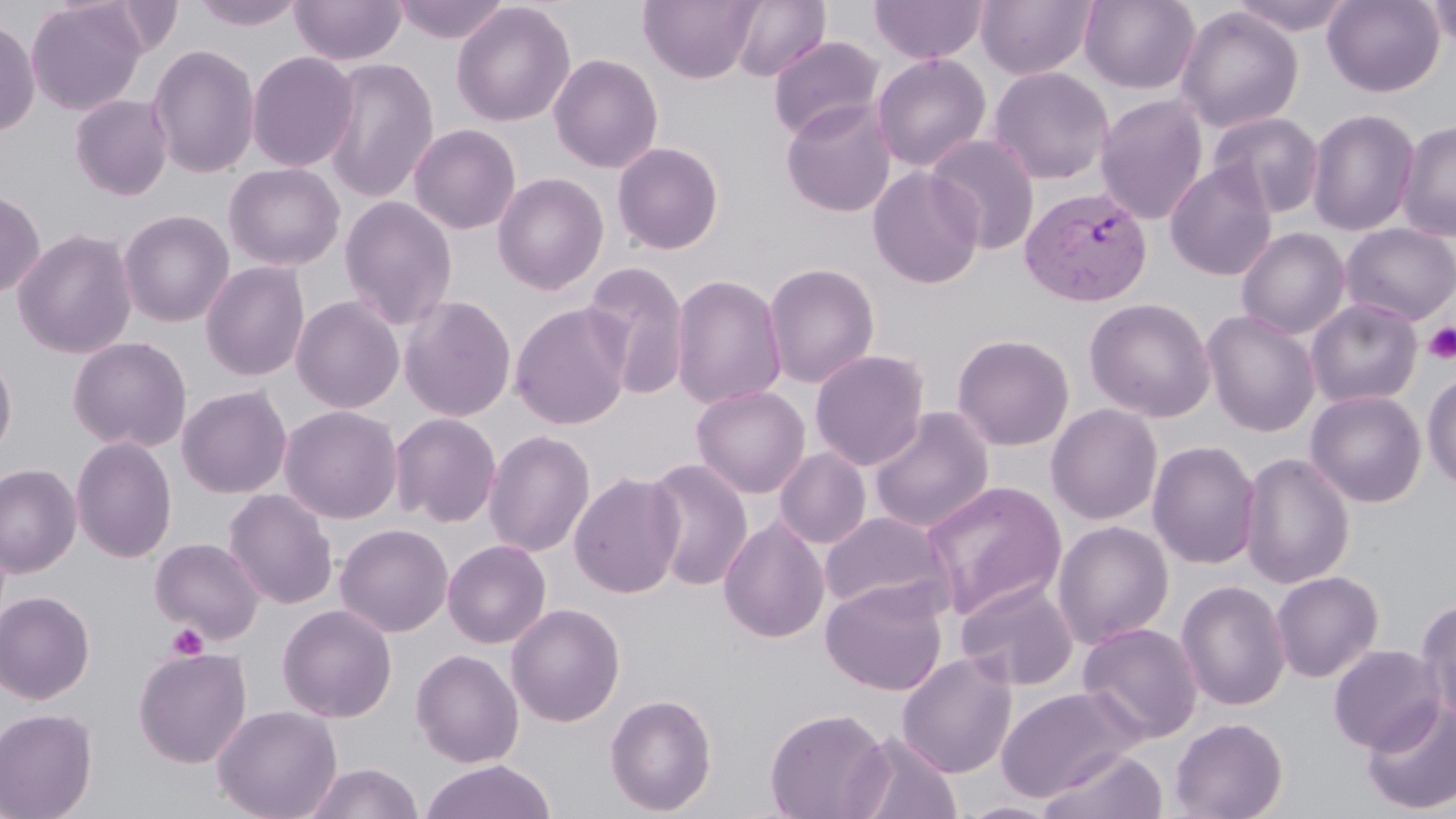
slide_level_diagnosis: Plasmodium vivax
platelet_locations: 'approximate bounding boxes as (x1,y1)-(x2,y2) corner pairs in pixels: (1423,322)-(1456,364), (167,622)-(209,659)'
preparation: thin blood smear
field_of_view: single
modality: light microscopy
image_size: 1456×819 pixels
uninfected_red_blood_cell_locations: 'approximate bounding boxes as (x1,y1)-(x2,y2) corner pairs in pixels: (25,0)-(147,115), (289,0)-(407,66), (392,0)-(509,44), (638,0)-(763,84), (868,0)-(988,64), (975,0)-(1096,81), (1079,0)-(1200,93), (1227,0)-(1358,35), (1322,0)-(1445,97), (1425,0)-(1456,51), (192,1)-(306,31), (729,1)-(830,82), (451,2)-(576,128), (1175,6)-(1303,133), (0,16)-(40,138), (768,36)-(885,143), (147,44)-(261,179), (246,50)-(360,172), (548,53)-(664,174), (871,53)-(992,172), (321,57)-(440,204), (987,66)-(1115,185), (69,94)-(173,201), (1095,94)-(1209,225), (780,100)-(898,218), (1306,108)-(1419,237), (1207,112)-(1325,219), (1396,119)-(1456,242), (409,124)-(521,234), (926,134)-(1041,254), (611,141)-(725,255), (223,162)-(346,271), (1165,162)-(1277,281), (866,166)-(985,290), (492,172)-(609,295), (500,172)-(615,429), (0,188)-(45,299), (339,195)-(457,329), (118,209)-(235,327), (1340,223)-(1456,326), (1236,227)-(1350,340), (12,228)-(137,359), (199,261)-(310,382), (582,261)-(690,400), (763,262)-(880,388), (670,273)-(787,411), (290,295)-(405,413), (398,295)-(517,422), (1083,297)-(1215,422), (1305,298)-(1423,408), (509,302)-(633,430), (1202,309)-(1320,436), (952,333)-(1075,451), (67,336)-(192,452), (0,348)-(18,462), (809,349)-(931,471), (1422,371)-(1456,489), (690,384)-(810,498), (176,385)-(293,498), (1305,389)-(1427,508), (1046,403)-(1162,525), (279,405)-(403,524), (868,407)-(994,534), (389,412)-(502,527), (483,429)-(595,557), (70,436)-(177,563), (1147,440)-(1262,569), (774,448)-(872,549), (1239,451)-(1356,589), (643,458)-(753,591), (0,463)-(82,578), (569,471)-(685,599), (921,480)-(1067,620), (223,488)-(338,609), (819,511)-(954,616), (718,516)-(830,644), (1051,520)-(1175,649), (335,523)-(453,637), (149,537)-(265,643), (442,539)-(552,649), (1270,571)-(1384,683), (955,579)-(1080,691), (820,580)-(948,696), (1175,580)-(1291,711), (0,590)-(96,705), (1415,597)-(1456,725), (506,602)-(625,727), (277,604)-(397,723), (1077,622)-(1204,744), (1328,643)-(1446,754), (133,646)-(252,768), (410,648)-(524,768), (897,653)-(1017,778), (996,685)-(1145,804), (605,693)-(718,815), (1360,698)-(1456,815), (211,704)-(342,819), (0,707)-(98,819), (765,707)-(892,819), (1170,717)-(1289,819), (845,731)-(963,819), (1037,748)-(1169,819), (418,760)-(558,819), (303,762)-(424,819), (956,800)-(1064,818)'
magnification: 1000x
stain: May-Grünwald-Giemsa
plasmodium_vivax_infected_red_blood_cell_locations: 'approximate bounding boxes as (x1,y1)-(x2,y2) corner pairs in pixels: (1020,186)-(1153,306)'